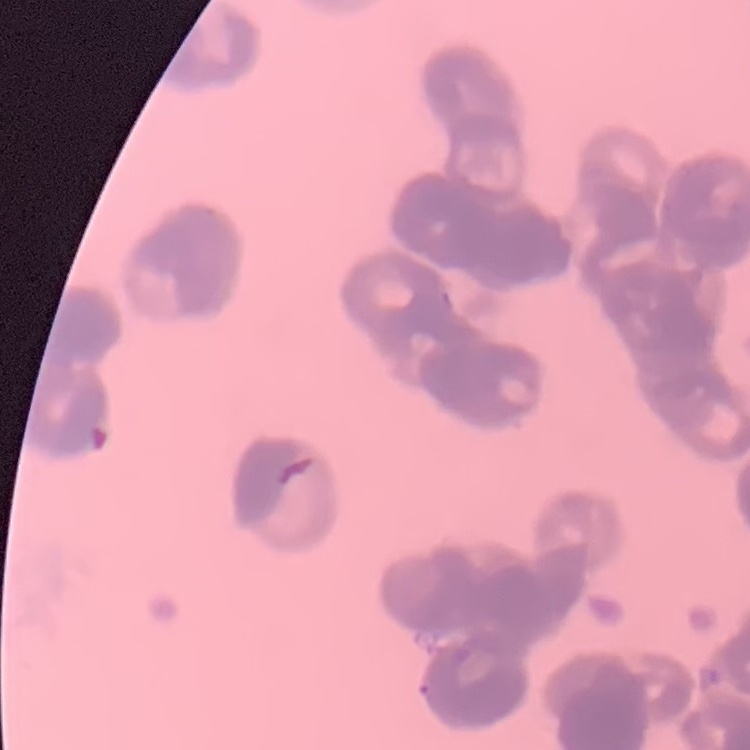
Summary:
  - Red blood cell morphology: rouleaux formation
  - Preparation: thin blood smear
  - Image type: square crop of a larger photomicrograph
  - Stain: Field's or Giemsa